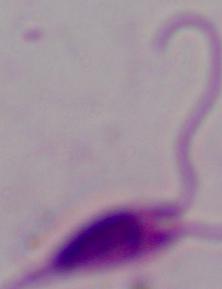
Summary:
  - Modality: micrograph
  - Magnification: 1000x
  - Identification: Leishmania